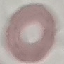

Malaria status: uninfected. Cell patch, automatically extracted from a larger field of view and resized to 64 × 64 pixels. Photographed with a smartphone camera at the microscope eyepiece. Giemsa-stained preparation. Thin blood film.